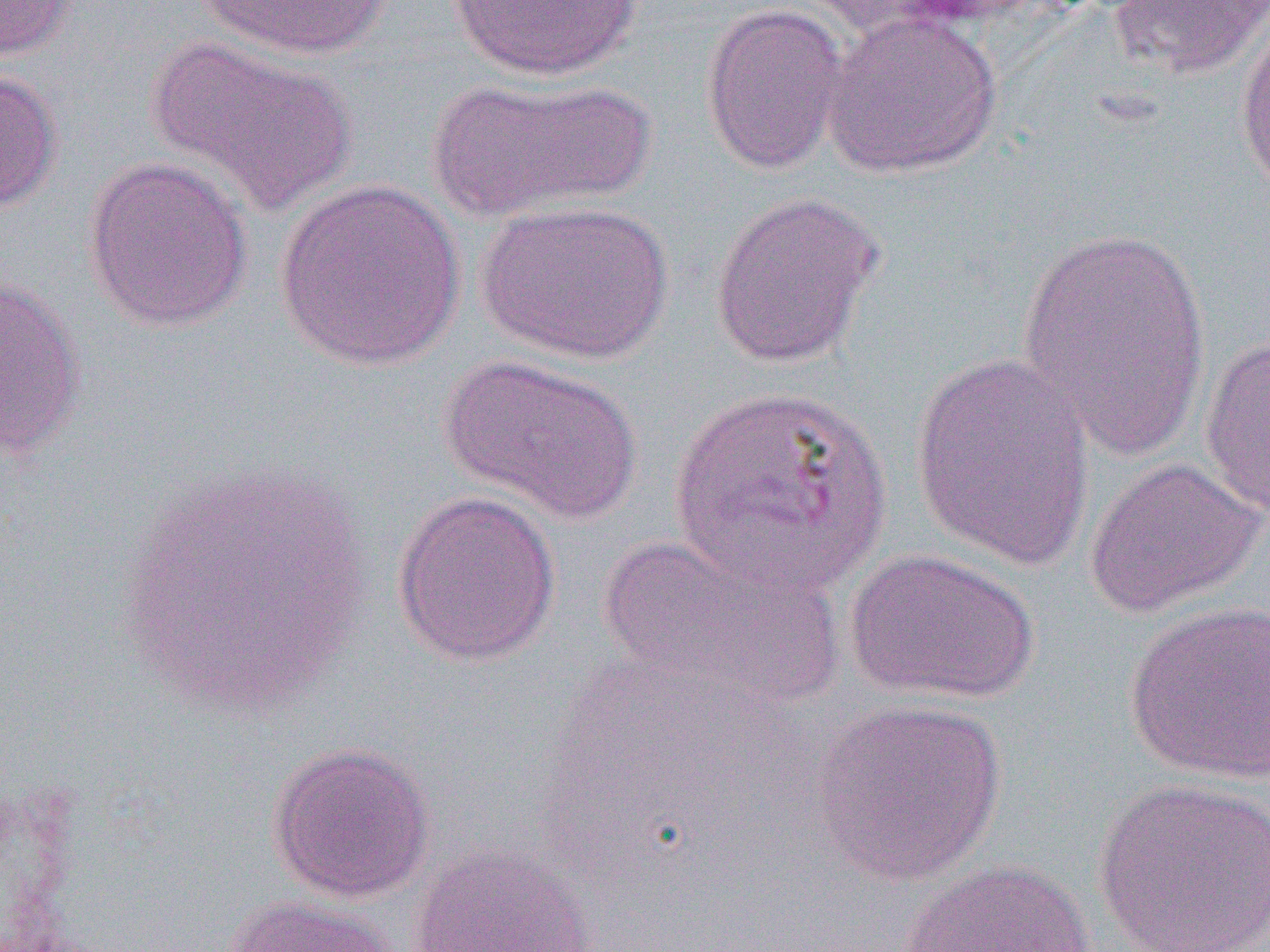
slide_level_diagnosis: Plasmodium vivax
preparation: thin blood film
magnification: 1000x
uninfected_red_blood_cell_locations: 'approximate bounding boxes as [x1, y1, x2, y2] in pixels: [0, 0, 78, 62], [196, 0, 395, 61], [448, 0, 643, 81], [1107, 0, 1269, 80], [700, 3, 849, 176], [821, 9, 1002, 180], [1234, 12, 1270, 196], [145, 36, 357, 220], [0, 66, 63, 213], [426, 75, 655, 222], [82, 156, 253, 332], [274, 179, 466, 371], [708, 190, 885, 369], [474, 199, 675, 365], [1015, 222, 1214, 460], [0, 275, 86, 461], [1199, 335, 1270, 517], [910, 350, 1097, 571], [438, 353, 643, 525], [667, 382, 892, 598], [1083, 456, 1267, 619], [115, 458, 374, 719], [391, 490, 560, 667], [597, 531, 842, 712], [842, 547, 1041, 705], [1123, 600, 1270, 785], [810, 697, 1008, 886], [266, 740, 436, 904], [1094, 777, 1270, 952], [407, 845, 598, 952], [896, 857, 1098, 951], [220, 894, 398, 952]'
image_size: 1270×952 pixels
modality: optical microscopy
field_of_view: single